Comment on the morphology of the erythrocytes.
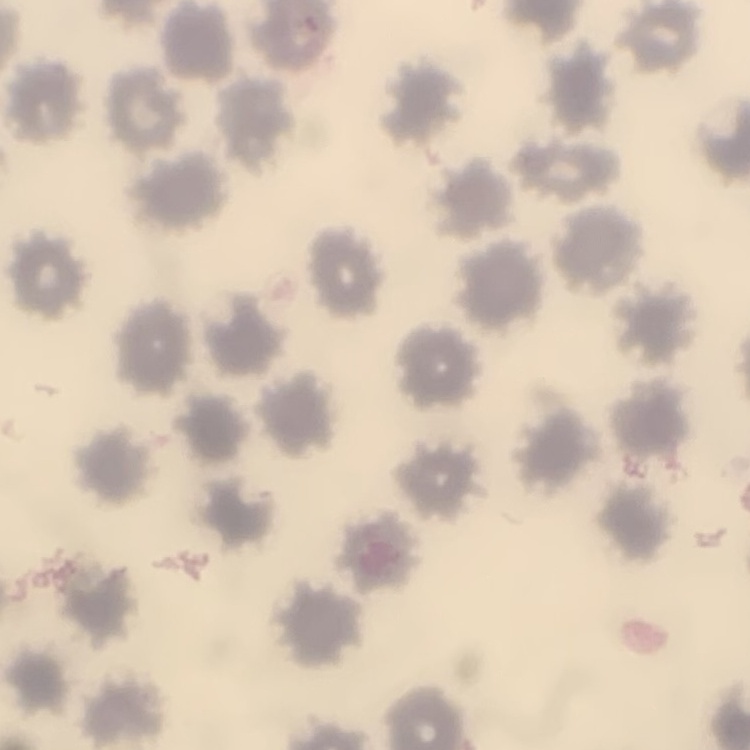

No rouleaux formation.

stain = Field's or Giemsa
image type = one tile cut from a larger photomicrograph
preparation = thin peripheral smear